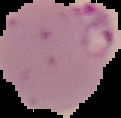

The area outside the segmented cell region is set to black. Result: malaria parasites identified. From a thin blood smear. Image is 121×118 pixels.